Name the blood parasite species.
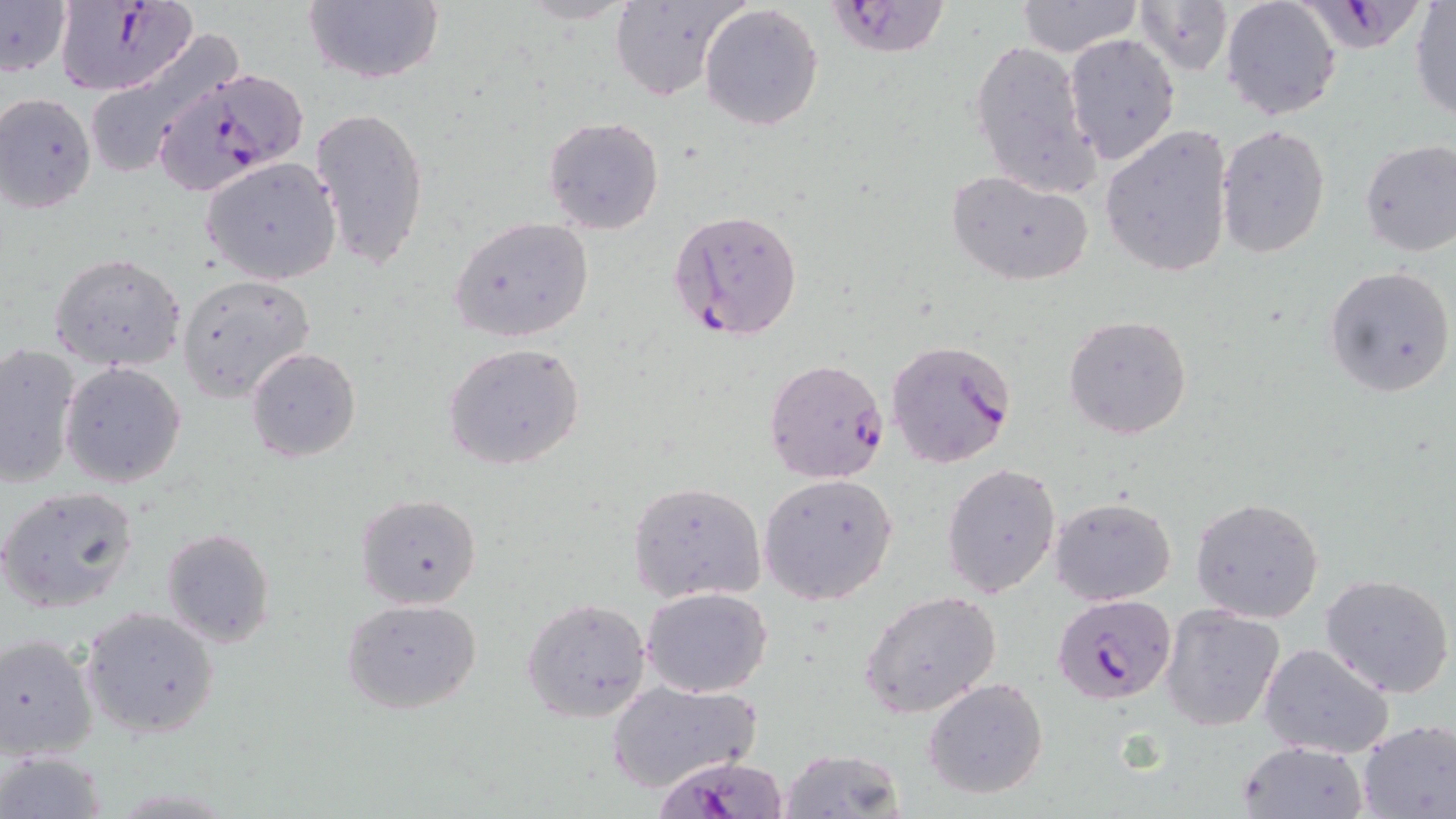

Plasmodium falciparum.

field of view = one of a larger specimen
preparation = thin blood smear
modality = optical microscopy
magnification = 1000x
stain = May-Grünwald-Giemsa
image size = 1456×819 pixels
uninfected red blood cell locations (subset) = approximate bounding boxes as (x1,y1)-(x2,y2) corner pairs in pixels: (301,0)-(446,87), (514,0)-(639,25), (605,0)-(746,101), (1014,0)-(1143,56), (1133,0)-(1233,78), (1221,0)-(1342,120), (0,1)-(71,77), (1409,2)-(1456,120), (699,4)-(824,132), (78,31)-(241,182), (1063,32)-(1181,166), (968,38)-(1099,197), (0,93)-(98,214), (311,104)-(431,274), (543,117)-(665,235), (1100,123)-(1235,280), (1216,124)-(1330,258), (1358,139)-(1456,257), (201,157)-(343,285), (945,169)-(1095,287), (449,215)-(595,343), (49,250)-(187,371), (1323,265)-(1455,398), (176,273)-(315,402), (1063,314)-(1194,441), (442,342)-(586,471), (0,343)-(80,487), (246,347)-(360,461), (60,363)-(187,488), (941,461)-(1063,599), (758,473)-(899,606), (628,481)-(766,602), (0,485)-(142,616), (353,492)-(483,610), (1048,496)-(1177,604), (1190,496)-(1325,624), (160,527)-(275,648), (1320,572)-(1455,698), (642,586)-(772,697), (862,590)-(1003,718), (341,597)-(483,714), (523,598)-(650,721), (1160,605)-(1285,731), (80,606)-(220,740), (0,632)-(99,761), (1257,642)-(1396,759), (923,677)-(1049,800), (606,679)-(761,793), (1356,718)-(1456,819), (1238,739)-(1367,819), (777,748)-(907,819), (0,750)-(108,816)
Plasmodium falciparum-infected red blood cell locations (subset) = approximate bounding boxes as (x1,y1)-(x2,y2) corner pairs in pixels: (52,0)-(197,96), (825,1)-(953,57), (1308,1)-(1418,60), (146,64)-(308,199), (669,208)-(803,343), (885,339)-(1019,471), (764,358)-(890,483), (645,739)-(786,819)